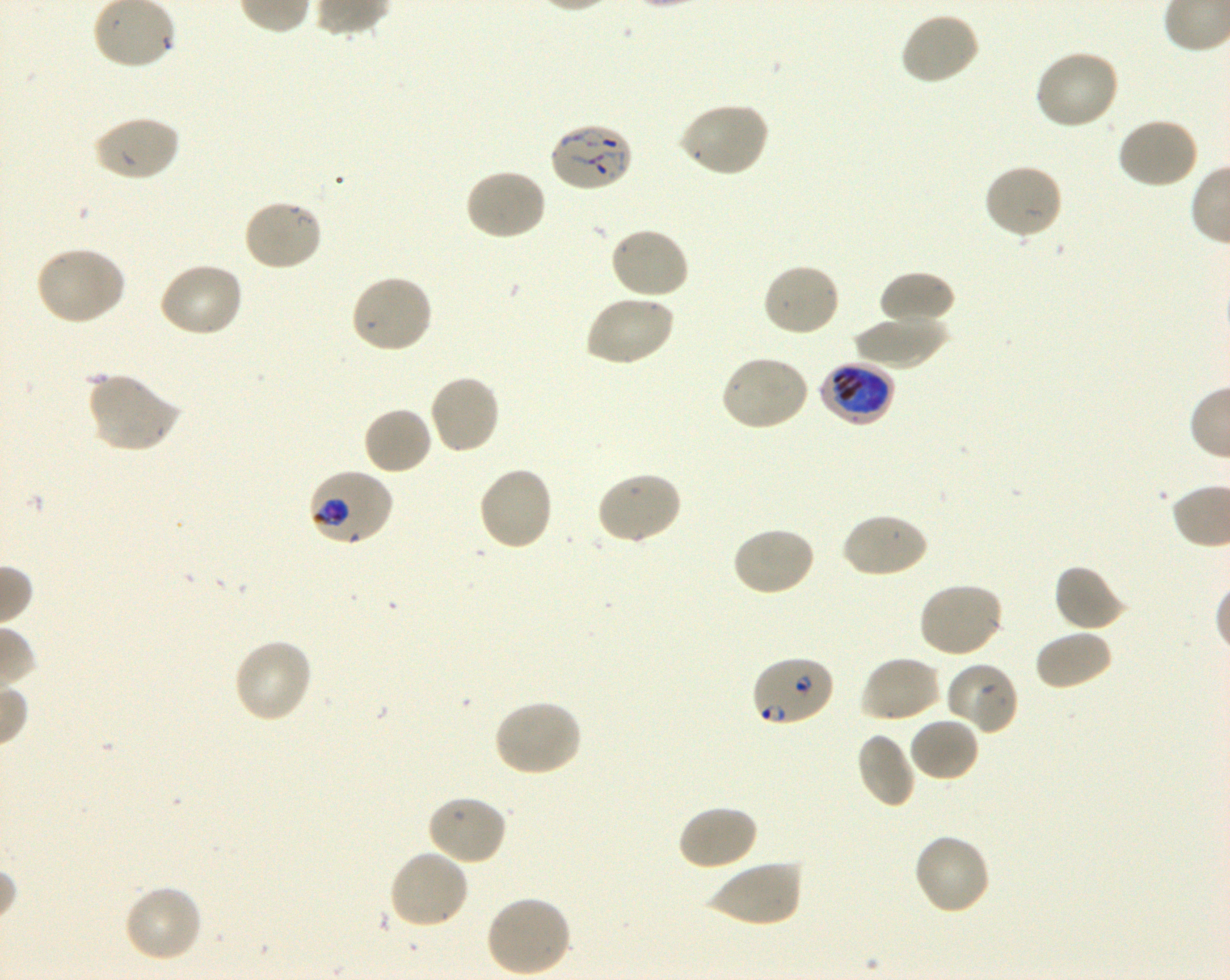
Approximate bounding boxes as (x1, y1, x2, y2) in pixels. Not every red blood cell is marked. A life-cycle stage — or a range of stages, where the recorded stages span more than one — follows each staged infected red blood cell.
Summary:
  - Locations of uninfected red blood cells: (899, 11, 981, 86), (1033, 49, 1121, 131), (677, 101, 770, 178), (91, 115, 180, 183), (1115, 115, 1200, 190), (983, 162, 1065, 240), (463, 167, 547, 242), (242, 198, 324, 272), (608, 226, 691, 300), (34, 246, 126, 326), (157, 261, 244, 338), (761, 262, 842, 337), (877, 270, 956, 329), (350, 273, 434, 355), (583, 292, 675, 367), (852, 314, 948, 369), (719, 355, 810, 432), (88, 372, 182, 454), (428, 374, 501, 456), (362, 406, 433, 476), (477, 465, 554, 553), (595, 471, 683, 546), (841, 511, 929, 579), (731, 526, 816, 597), (1053, 563, 1127, 633), (916, 582, 1005, 659), (1033, 629, 1112, 691), (232, 636, 314, 724), (859, 655, 942, 724), (944, 661, 1019, 735), (492, 699, 582, 777), (908, 716, 980, 783), (856, 732, 916, 809), (425, 793, 508, 866), (677, 803, 758, 871), (912, 832, 992, 917), (387, 847, 470, 930), (707, 858, 803, 928), (122, 884, 202, 964), (484, 894, 573, 977)
  - Locations of infected red blood cells: (549, 123, 634, 193); (817, 362, 896, 423) late trophozoite to early schizont; (308, 468, 395, 548) trophozoite; (751, 655, 836, 727) ring
  - Life-cycle stages observed: ring, trophozoite
  - Objective: 100x, oil immersion, numerical aperture 1.30
  - Field of view: one from this slide
  - Image size: 1230×980 pixels
  - Culture: P. falciparum strain 3D7, shaking, in vitro
  - Preparation: thin blood film
  - Stain: Giemsa
  - Donor blood group: O+